Identify the parasite.
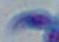

This is Toxoplasma gondii.

Summary:
  - Modality: photomicrograph
  - Magnification: 1000x